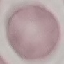
Summary:
  - Result: no malaria parasites detected
  - Stain: Giemsa
  - Image type: automatically extracted cell patch, resized to 64 × 64 pixels
  - Preparation: thin blood smear
  - Capture: smartphone through the microscope eyepiece